Assess this cell for malaria.
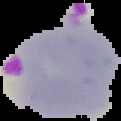

Parasitized.

From a thin blood film. The area outside the segmented cell region is set to black. Image is 121×121 pixels.